Describe the morphology of the erythrocytes.
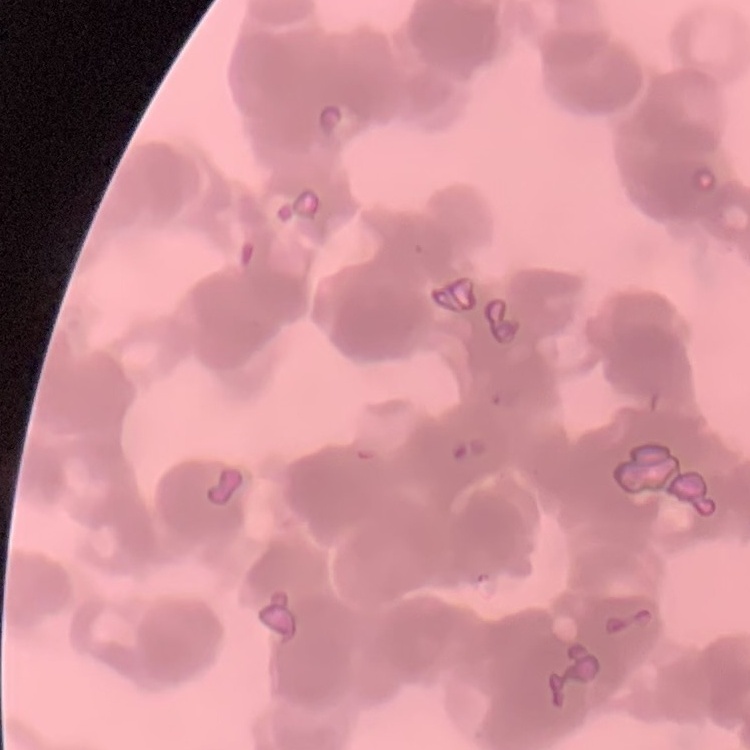

They show rouleaux formation.

Summary:
  - Preparation: thin blood smear
  - Stain: Field's or Giemsa
  - Image type: one tile cut from a larger photomicrograph